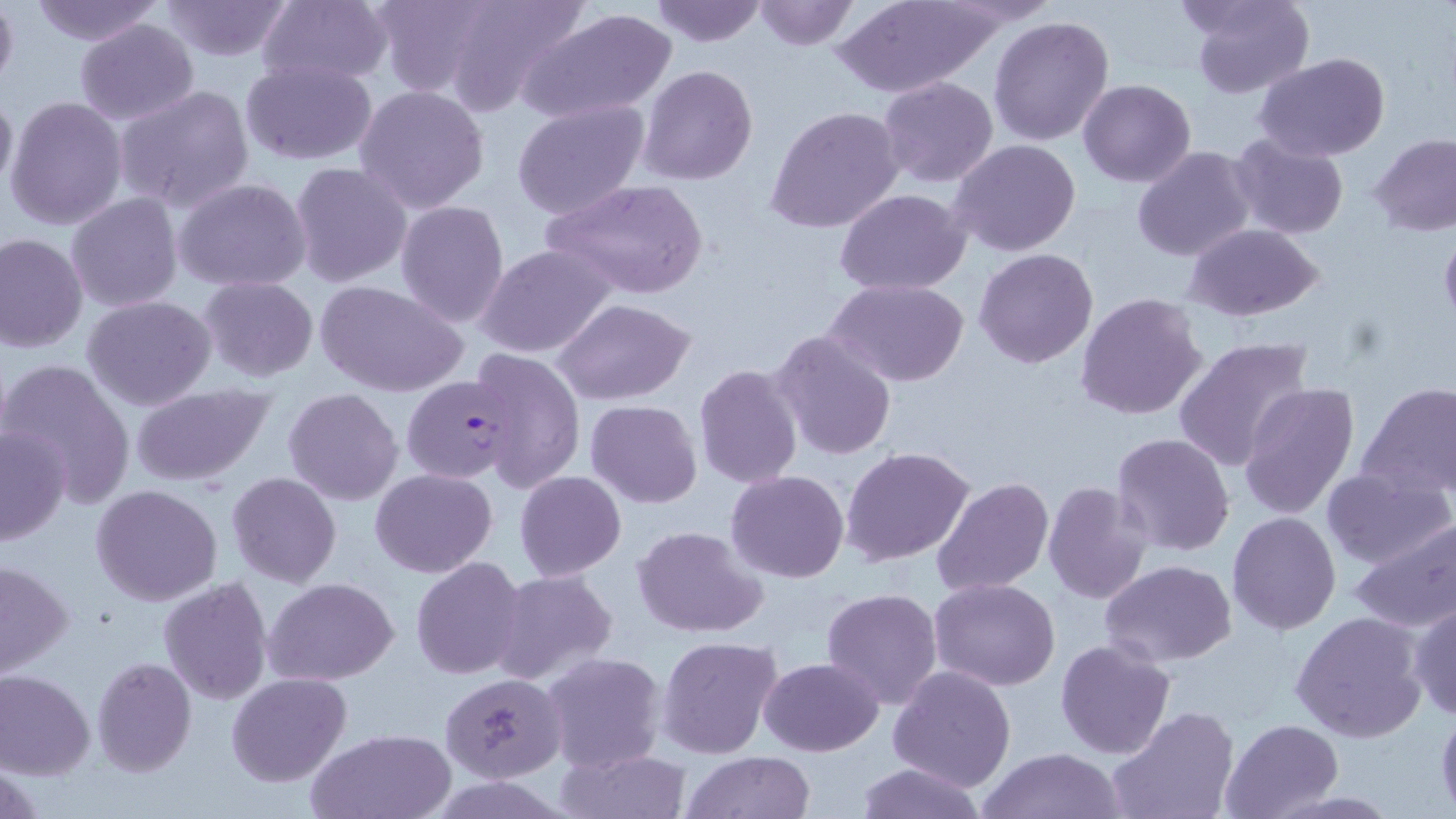
{
  "slide_level_diagnosis": "Plasmodium falciparum",
  "field_of_view": "one of a larger specimen",
  "image_size": "1456×819 pixels",
  "magnification": "1000x",
  "plasmodium_falciparum_infected_red_blood_cell_locations": "approximate bounding boxes as (x1, y1, x2, y2) in pixels: (401, 373, 516, 486)",
  "preparation": "thin blood film",
  "stain": "May-Grünwald-Giemsa",
  "uninfected_red_blood_cell_locations": "approximate bounding boxes as (x1, y1, x2, y2) in pixels: (0, 0, 18, 94), (156, 0, 297, 61), (367, 0, 498, 97), (436, 0, 590, 116), (647, 0, 767, 47), (834, 0, 1000, 97), (1187, 0, 1314, 99), (23, 1, 167, 46), (254, 1, 394, 89), (750, 1, 859, 49), (517, 7, 678, 125), (987, 15, 1115, 147), (75, 18, 199, 125), (1254, 54, 1388, 162), (240, 59, 379, 166), (639, 64, 757, 186), (877, 75, 999, 188), (1078, 79, 1196, 186), (0, 83, 17, 201), (353, 83, 492, 214), (113, 84, 257, 213), (5, 95, 128, 232), (512, 100, 650, 222), (765, 105, 906, 234), (1226, 133, 1349, 240), (1370, 133, 1456, 235), (949, 139, 1080, 257), (1133, 145, 1256, 263), (289, 161, 413, 288), (173, 177, 313, 291), (543, 177, 709, 300), (835, 189, 971, 295), (66, 193, 182, 312), (395, 200, 509, 328), (1186, 224, 1325, 322), (1, 232, 87, 353), (473, 244, 618, 358), (974, 248, 1099, 368), (198, 275, 319, 385), (313, 279, 469, 400), (825, 279, 970, 386), (1076, 292, 1208, 422), (82, 295, 216, 411), (553, 297, 697, 405), (766, 328, 898, 462), (1173, 336, 1313, 472), (465, 347, 584, 492), (2, 358, 138, 507), (692, 364, 804, 490), (1357, 381, 1456, 498), (1239, 384, 1363, 520), (129, 385, 276, 488), (283, 388, 403, 505), (586, 399, 703, 507), (0, 425, 72, 546), (1110, 433, 1236, 556), (841, 446, 976, 567), (1321, 467, 1454, 571), (370, 468, 497, 578), (725, 470, 851, 583), (514, 471, 626, 579), (227, 472, 341, 587), (931, 475, 1055, 596), (1043, 479, 1155, 605), (90, 484, 222, 605), (1227, 511, 1341, 633), (1348, 518, 1456, 634), (633, 526, 768, 638), (411, 556, 527, 680), (0, 558, 75, 678), (1101, 559, 1238, 666), (493, 570, 618, 685), (157, 576, 272, 706), (265, 577, 400, 684), (929, 577, 1061, 691), (821, 588, 944, 710), (1406, 600, 1456, 721), (1289, 611, 1426, 744), (657, 635, 782, 758), (1054, 638, 1177, 759), (541, 651, 668, 774), (759, 656, 883, 756), (91, 657, 197, 776), (887, 664, 1018, 792), (0, 669, 96, 779), (441, 671, 566, 783), (226, 673, 350, 787), (1107, 705, 1239, 819), (1435, 706, 1456, 812), (1220, 718, 1344, 817), (306, 728, 456, 818), (560, 747, 690, 819), (976, 748, 1124, 819), (682, 751, 817, 818), (852, 761, 989, 819)",
  "modality": "light microscopy"
}